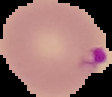
From a thin blood smear. Cell region segmented out of the field of view; the surrounding area is masked to black. Image is 112×97 pixels. Malaria status: parasitized.